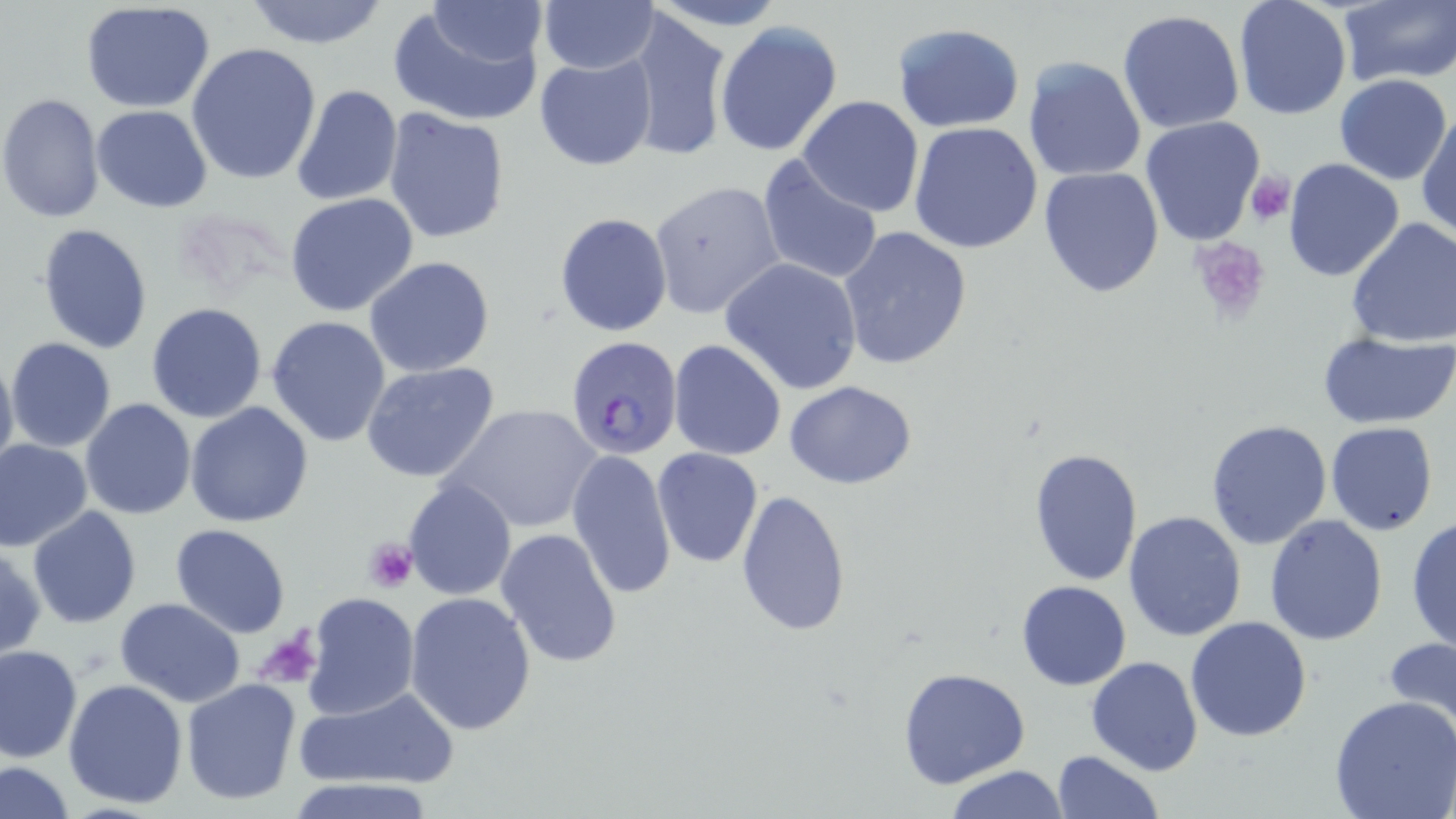
slide-level diagnosis = Plasmodium falciparum
modality = optical microscopy
platelet locations = approximate bounding boxes as (x1,y1)-(x2,y2) corner pairs in pixels: (1244,170)-(1295,225), (1189,237)-(1271,321), (361,536)-(419,594), (258,629)-(323,690)
magnification = 1000x
stain = May-Grünwald-Giemsa
field of view = single
uninfected red blood cell locations = approximate bounding boxes as (x1,y1)-(x2,y2) corner pairs in pixels: (423,0)-(552,67), (1232,0)-(1353,121), (79,1)-(215,113), (239,1)-(393,49), (539,1)-(657,74), (1335,1)-(1456,86), (388,4)-(546,127), (622,6)-(731,164), (1117,9)-(1246,135), (714,20)-(842,157), (894,24)-(1024,131), (187,42)-(322,185), (533,53)-(657,171), (1022,55)-(1147,183), (1333,73)-(1453,185), (289,84)-(402,208), (0,93)-(105,223), (296,93)-(501,225), (797,95)-(924,216), (92,105)-(213,213), (794,106)-(1037,232), (383,108)-(510,246), (1416,108)-(1456,240), (1139,117)-(1268,248), (909,120)-(1042,254), (757,153)-(886,287), (1282,157)-(1405,284), (1039,166)-(1165,299), (649,181)-(786,320), (285,193)-(419,316), (555,213)-(671,336), (1345,218)-(1456,349), (37,223)-(155,355), (837,226)-(972,372), (365,256)-(495,376), (720,257)-(863,394), (146,302)-(267,423), (266,316)-(392,448), (1317,330)-(1456,430), (6,338)-(117,453), (668,339)-(787,461), (0,348)-(18,483), (361,362)-(499,483), (785,380)-(917,489), (80,399)-(197,519), (185,402)-(314,528), (445,403)-(602,534), (1204,420)-(1333,551), (1325,422)-(1437,536), (0,438)-(93,552), (1029,446)-(1142,584), (652,448)-(762,568), (566,449)-(677,601), (403,477)-(516,601), (734,490)-(852,637), (26,505)-(140,628), (1124,511)-(1249,643), (1264,514)-(1387,646), (1405,515)-(1456,655), (172,523)-(291,637), (495,528)-(624,668), (0,544)-(46,661), (1016,581)-(1132,690), (303,591)-(418,721), (404,591)-(536,736), (115,598)-(246,707), (1186,616)-(1312,740), (1383,638)-(1456,741), (0,645)-(82,764), (1085,656)-(1205,776), (899,667)-(1031,790), (63,678)-(189,810), (181,678)-(301,805), (294,687)-(459,793), (1330,697)-(1456,819), (1050,750)-(1163,819), (2,761)-(74,817), (941,765)-(1071,819), (289,777)-(442,819)
Plasmodium falciparum-infected red blood cell locations = approximate bounding boxes as (x1,y1)-(x2,y2) corner pairs in pixels: (565,336)-(683,461)
preparation = thin blood film
image size = 1456×819 pixels